Locate every blood parasite and identify its species.
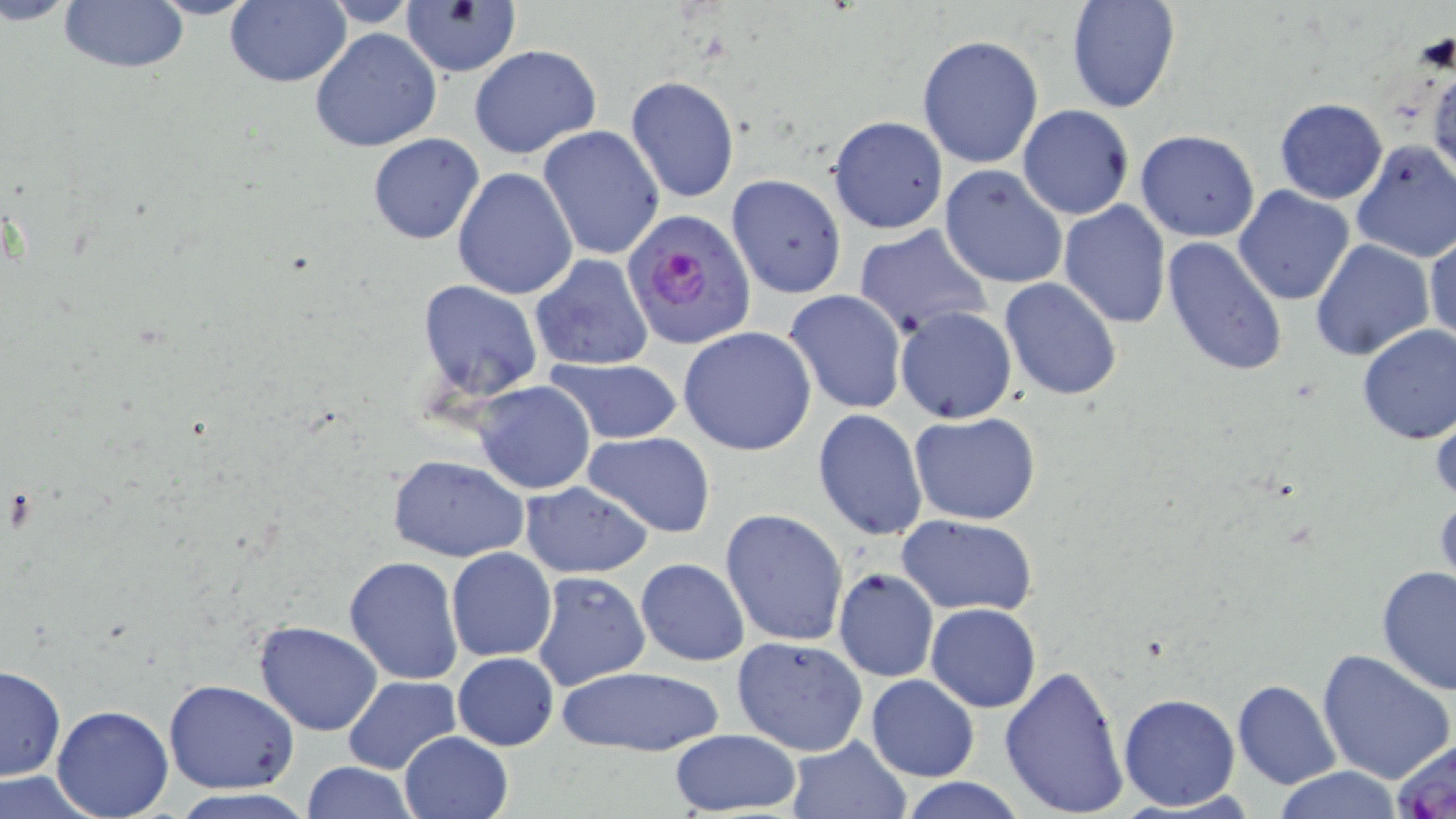
Approximate bounding boxes as [x1, y1, x2, y2] in pixels.
Plasmodium falciparum-infected red blood cells: [627, 209, 754, 347].
No Plasmodium ovale, Plasmodium malariae, Plasmodium vivax, Babesia divergens, or Trypanosoma brucei observed.

Summary:
  - Uninfected red blood cell locations: [59, 0, 188, 72], [143, 0, 262, 19], [224, 0, 349, 88], [316, 0, 425, 28], [1065, 0, 1181, 113], [400, 3, 522, 78], [309, 27, 442, 153], [916, 34, 1044, 170], [468, 44, 603, 160], [1426, 51, 1456, 188], [624, 77, 740, 203], [1273, 98, 1390, 204], [1017, 105, 1135, 220], [828, 115, 949, 235], [538, 125, 665, 260], [1134, 130, 1259, 242], [367, 132, 484, 245], [1350, 139, 1456, 262], [938, 165, 1068, 289], [452, 168, 579, 301], [727, 174, 846, 299], [1232, 184, 1356, 306], [1059, 200, 1171, 328], [852, 223, 993, 339], [1425, 230, 1456, 350], [1161, 237, 1289, 377], [1309, 237, 1435, 361], [529, 253, 654, 372], [999, 278, 1122, 402], [418, 281, 544, 402], [784, 291, 908, 413], [895, 307, 1017, 424], [1355, 324, 1456, 444], [678, 327, 817, 456], [543, 358, 684, 446], [472, 381, 596, 495], [1429, 395, 1456, 508], [812, 408, 927, 541], [909, 412, 1042, 526], [582, 432, 715, 536], [389, 456, 530, 563], [519, 480, 653, 580], [1433, 487, 1455, 595], [720, 508, 849, 648], [898, 516, 1038, 616], [446, 548, 558, 662], [344, 555, 465, 686], [634, 558, 749, 667], [1376, 566, 1456, 696], [833, 569, 938, 682], [531, 571, 652, 692], [926, 604, 1040, 713], [253, 620, 383, 736], [731, 635, 871, 757], [1315, 648, 1454, 786], [452, 652, 559, 750], [0, 665, 66, 782], [552, 666, 726, 758], [999, 666, 1128, 817], [343, 675, 461, 775], [867, 675, 979, 782], [164, 679, 298, 795], [1232, 679, 1341, 789], [1117, 692, 1241, 811], [52, 704, 173, 818], [667, 728, 802, 815], [398, 730, 512, 819], [1390, 734, 1456, 818], [785, 737, 912, 819], [301, 761, 417, 818], [1270, 767, 1404, 819], [0, 772, 111, 817], [898, 777, 1029, 818]
  - Slide-level diagnosis: Plasmodium falciparum
  - Stain: May-Grünwald-Giemsa
  - Image size: 1456×819 pixels
  - Magnification: 1000x
  - Preparation: thin blood smear
  - Field of view: one of a larger specimen
  - Modality: light microscopy